Classify this cell by malaria status.
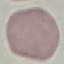
Uninfected.

Cell patch, automatically extracted from a larger field of view and resized to 64 × 64 pixels. Thin blood film. Giemsa-stained preparation. Acquired by smartphone through the microscope eyepiece.